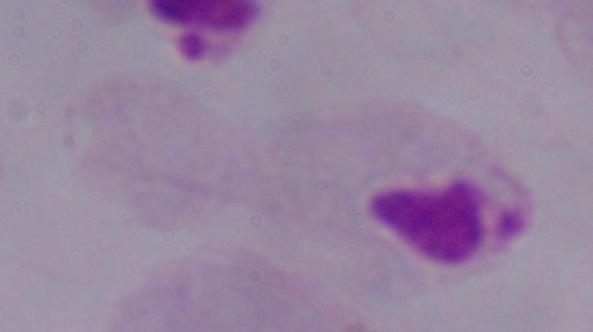
Summary:
  - Magnification: 1000x
  - Modality: photomicrograph
  - Identification: trichomonad